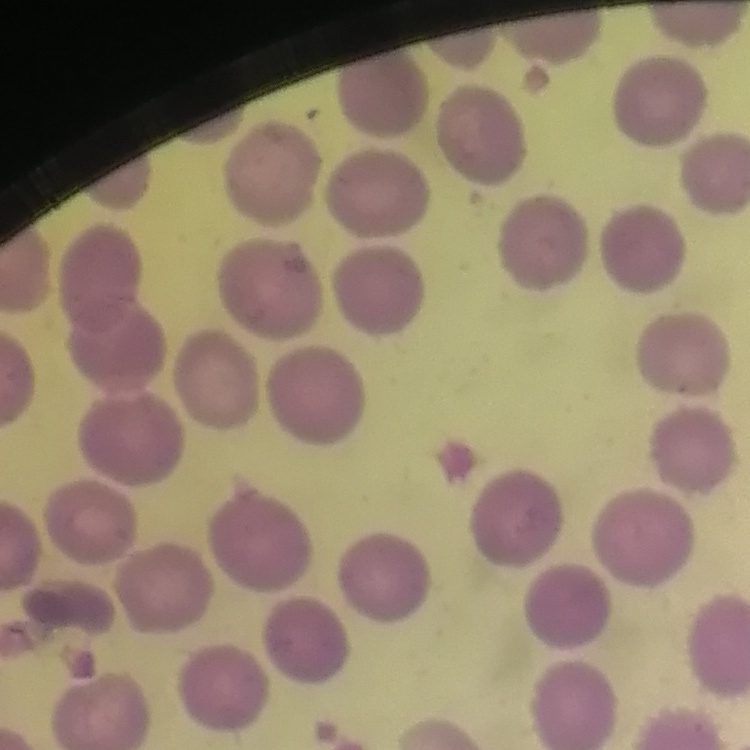

Summary:
  - Red blood cell morphology: no rouleaux formation
  - Preparation: thin blood film
  - Stain: Field's or Giemsa
  - Image type: one tile cut from a larger photomicrograph